Assess for malaria.
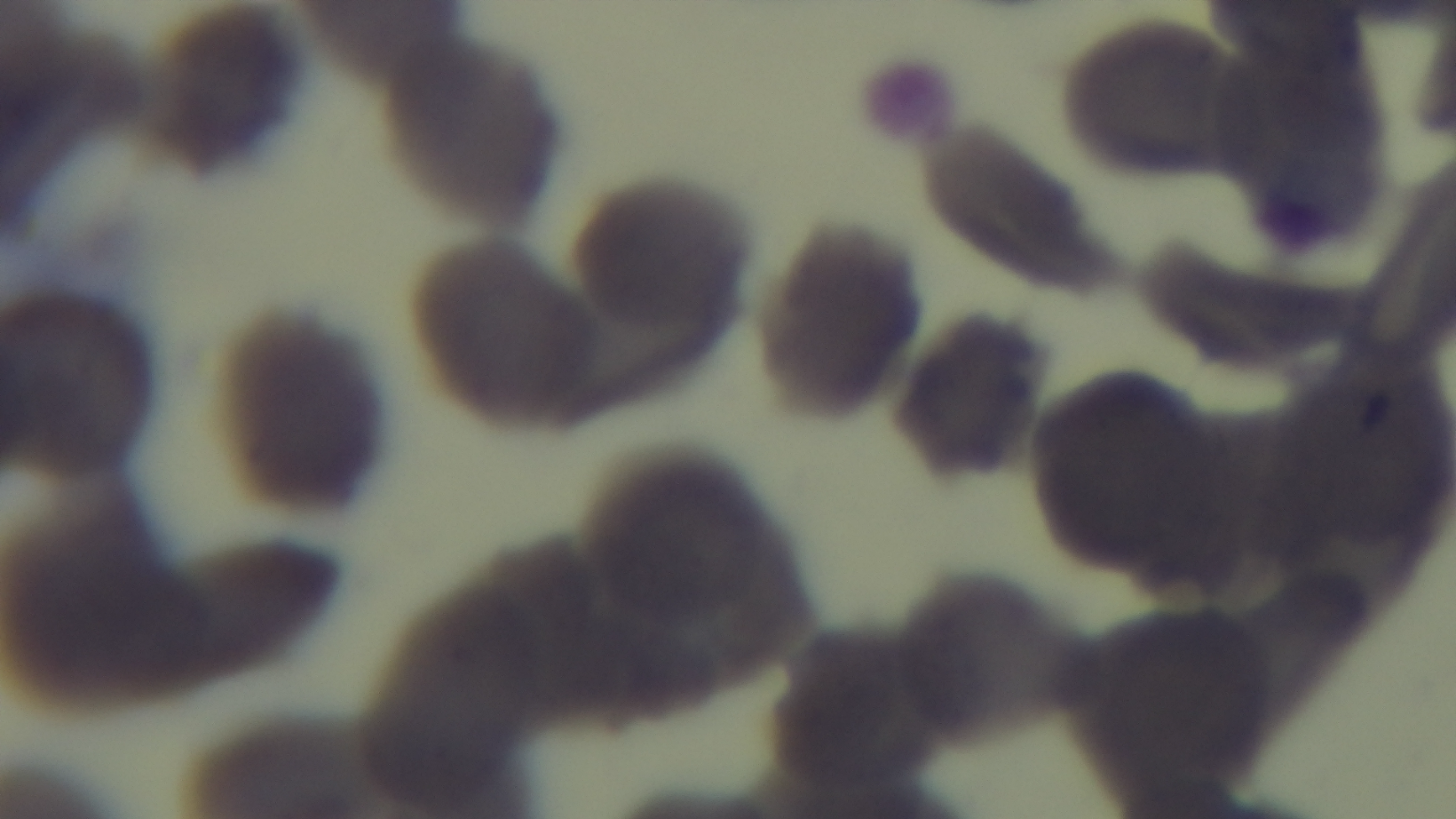

Uninfected.

stain = Giemsa
field of view = single
objective = 100x oil immersion
preparation = thin
capture = mounted 4K digital camera
modality = light microscopy